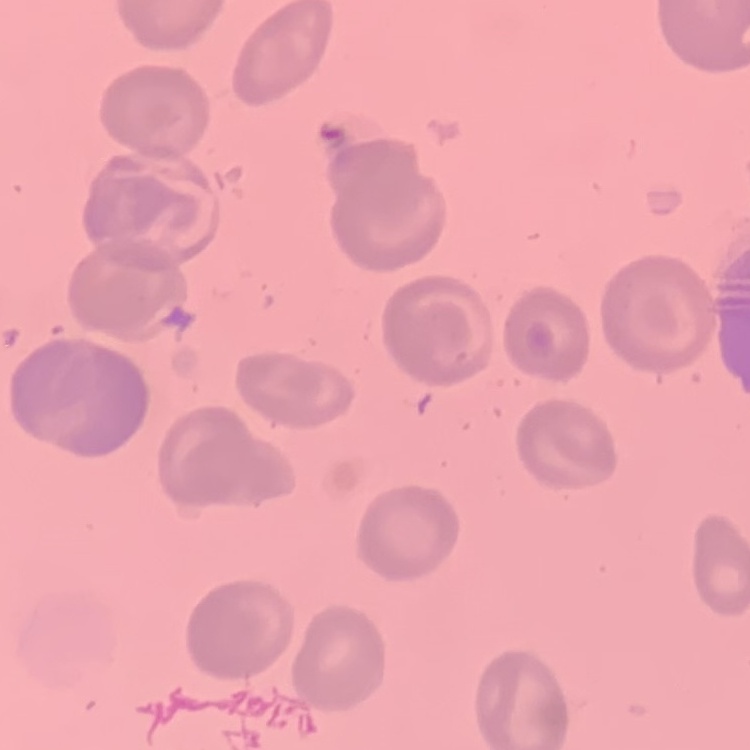

erythrocyte morphology = no rouleaux formation
preparation = thin peripheral smear
stain = Field's or Giemsa
image type = square crop of a larger photomicrograph